Classify this cell by malaria status.
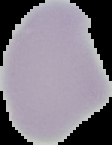
Uninfected.

{
  "image_size": "112×145 pixels",
  "preparation": "thin blood film",
  "image_type": "cell region segmented out of the field of view; surrounding area masked to black"
}